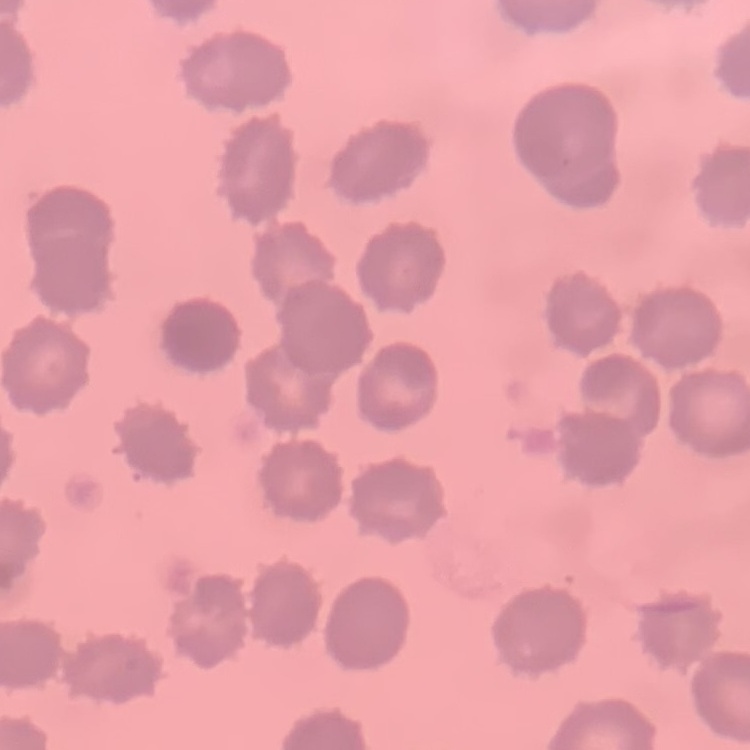
{
  "red_blood_cell_morphology": "no rouleaux formation",
  "image_type": "square crop of a larger photomicrograph",
  "stain": "Field's or Giemsa",
  "preparation": "thin blood film"
}